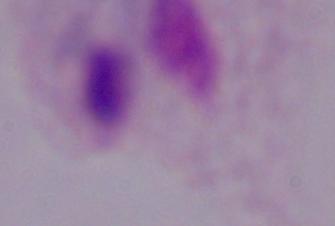

{
  "identification": "trichomonad",
  "modality": "photomicrograph",
  "magnification": "1000x"
}